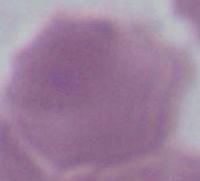
Summary:
  - Modality: micrograph
  - Identification: erythrocyte
  - Magnification: 1000x